Outline platelets.
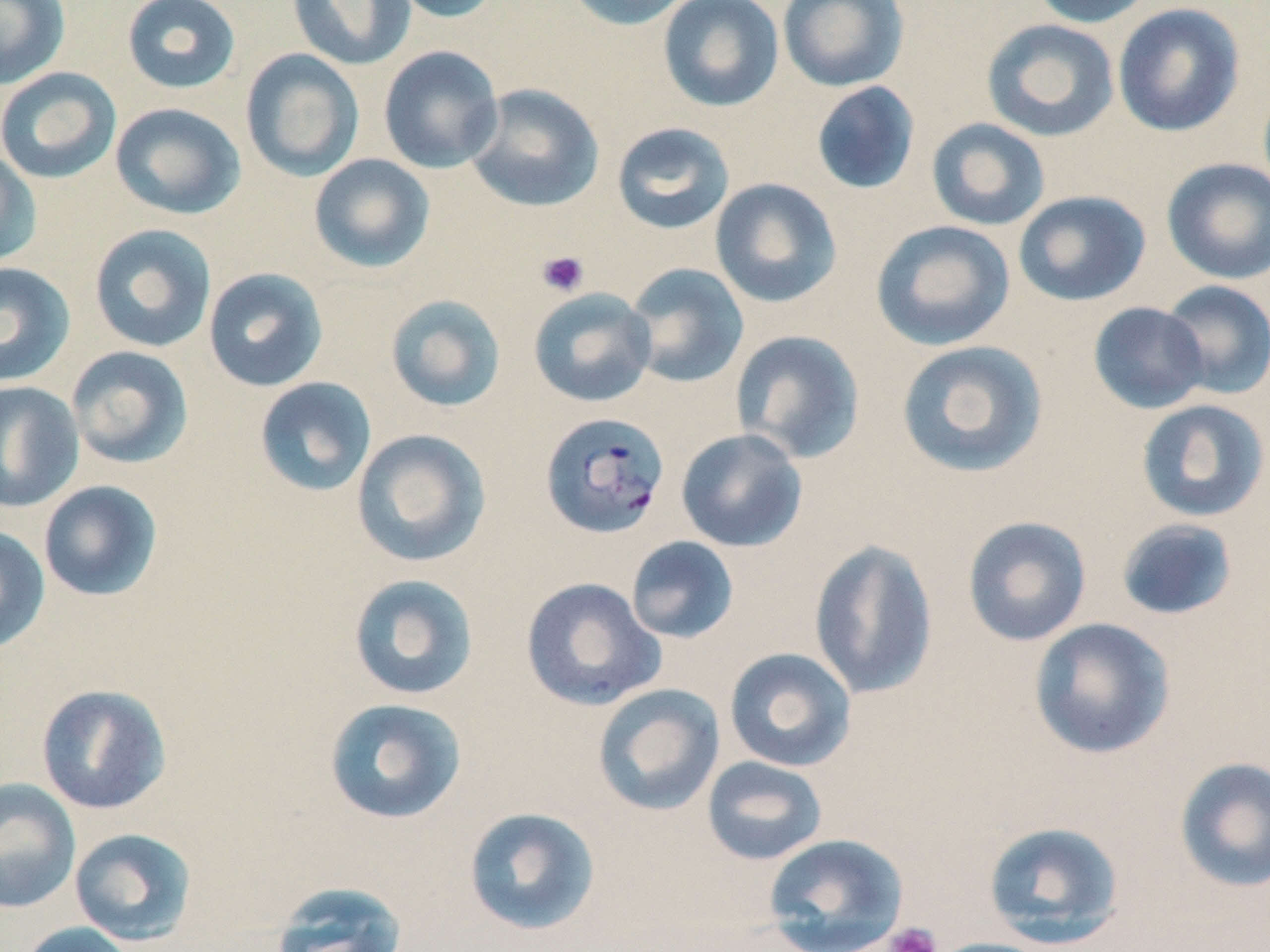

Approximate bounding boxes as (x1, y1, x2, y2) in pixels.
Platelets: (537, 250, 589, 297), (884, 923, 942, 952).

Summary:
  - Uninfected red blood cell locations: (0, 0, 70, 90), (121, 0, 241, 94), (287, 0, 416, 71), (384, 0, 502, 23), (561, 0, 696, 31), (657, 0, 784, 113), (777, 0, 909, 92), (1028, 0, 1158, 28), (1112, 3, 1245, 137), (981, 19, 1120, 142), (378, 45, 504, 173), (239, 49, 365, 183), (0, 67, 122, 184), (811, 81, 921, 195), (464, 83, 605, 213), (110, 102, 246, 220), (926, 118, 1051, 232), (611, 121, 735, 235), (0, 148, 41, 268), (308, 153, 436, 274), (1161, 157, 1270, 285), (709, 177, 843, 309), (1013, 190, 1151, 307), (870, 219, 1016, 351), (88, 223, 217, 353), (0, 262, 76, 387), (623, 262, 750, 389), (202, 267, 329, 393), (1159, 279, 1270, 401), (528, 287, 657, 408), (385, 294, 507, 413), (1088, 301, 1209, 414), (730, 330, 866, 464), (895, 339, 1050, 479), (65, 345, 194, 470), (254, 377, 377, 497), (0, 381, 84, 513), (1134, 399, 1270, 523), (351, 428, 491, 568), (675, 428, 808, 552), (38, 480, 163, 602), (962, 515, 1092, 647), (1115, 518, 1239, 622), (0, 524, 51, 655), (625, 536, 739, 645), (809, 539, 939, 699), (347, 572, 480, 701), (520, 576, 666, 712), (1028, 617, 1176, 760), (723, 647, 857, 772), (35, 683, 171, 815), (592, 683, 725, 816), (322, 697, 468, 825), (701, 755, 829, 866), (1173, 756, 1270, 894), (0, 777, 81, 914), (462, 806, 602, 936), (982, 820, 1126, 949), (68, 827, 199, 946), (762, 832, 909, 952), (267, 881, 410, 952), (18, 921, 139, 952), (924, 937, 1059, 952)
  - Plasmodium falciparum-infected red blood cell locations: (539, 410, 671, 539)
  - Slide-level diagnosis: Plasmodium falciparum
  - Field of view: single
  - Magnification: 1000x
  - Modality: optical microscopy
  - Preparation: thin blood film
  - Stain: May-Grünwald-Giemsa
  - Image size: 1270×952 pixels